Give the preparation type.
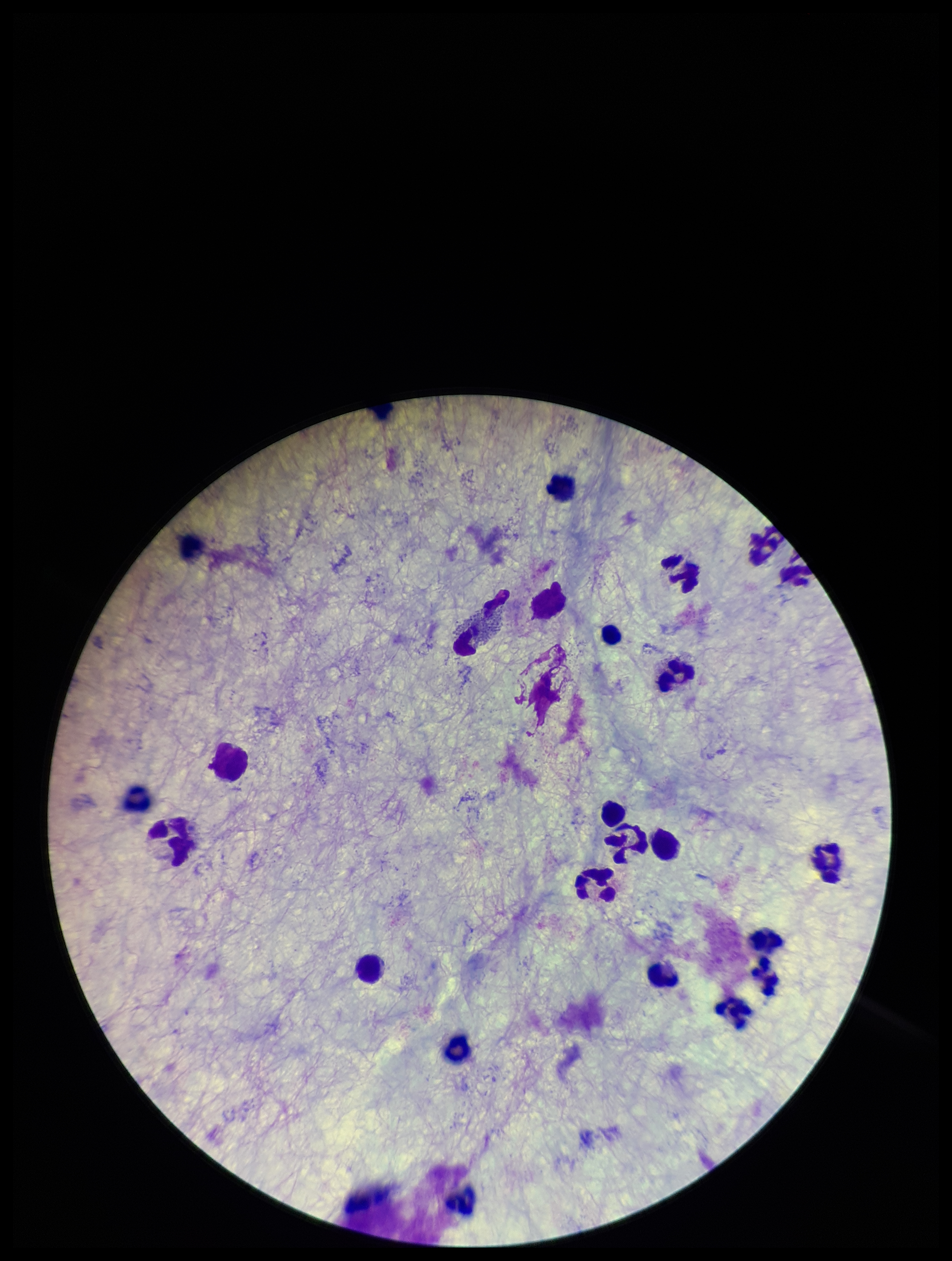

It is a thick blood smear.

{
  "plasmodium_parasites": "none identified",
  "field_of_view": "single",
  "parasite_count": 0,
  "image_size": "952×1261 pixels",
  "capture": "smartphone photograph through the microscope eyepiece",
  "stain": "Giemsa",
  "leukocyte_count": 21,
  "patient_malaria_status": "negative"
}